Identify the blood parasite species.
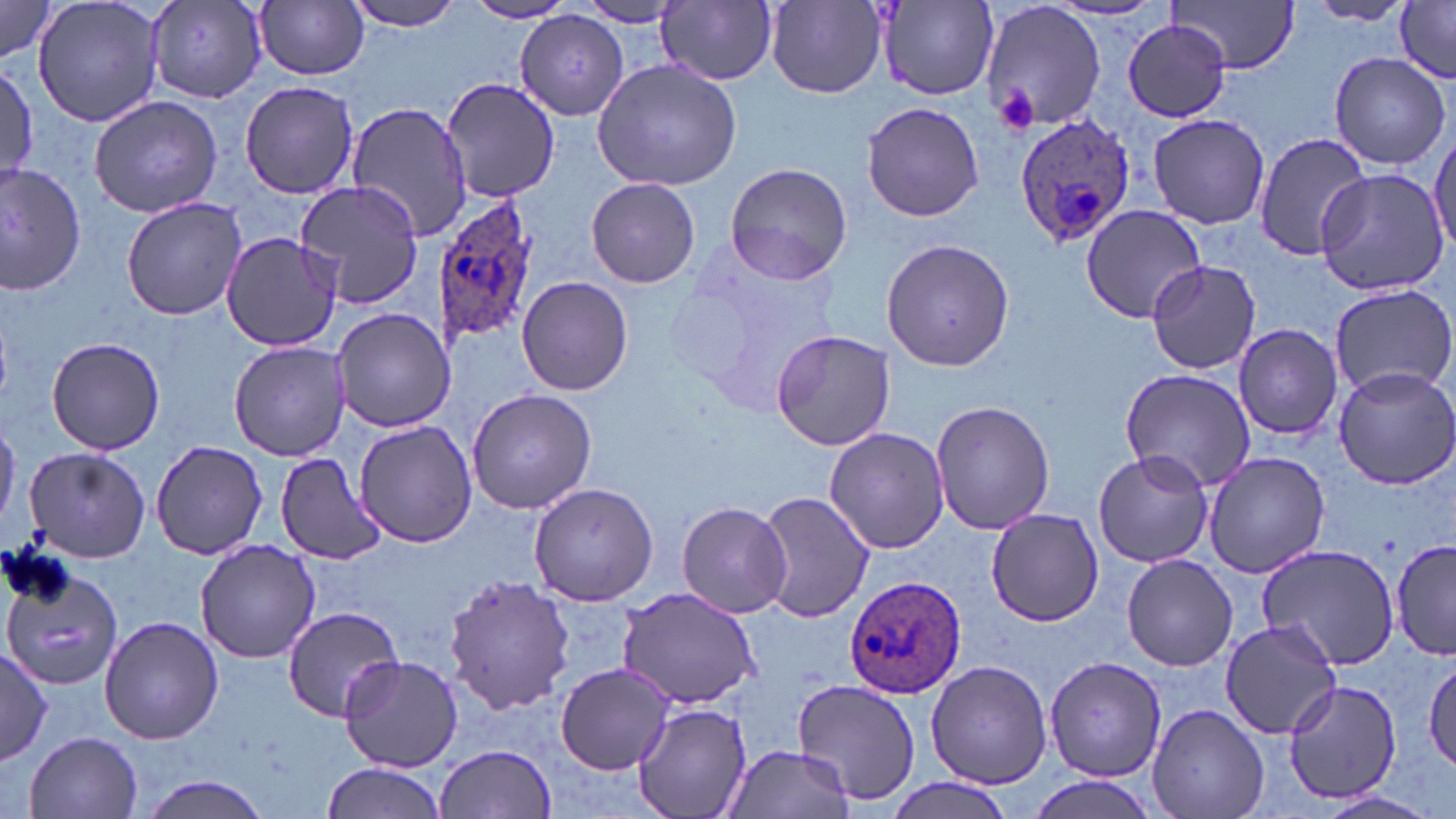
Plasmodium ovale.

image size = 1456×819 pixels
uninfected red blood cell locations = approximate bounding boxes as (x1, y1, x2, y2) in pixels: (31, 0, 165, 128), (345, 0, 471, 32), (876, 0, 997, 102), (145, 1, 270, 103), (767, 1, 888, 96), (981, 1, 1106, 135), (1168, 1, 1300, 74), (1301, 1, 1415, 24), (256, 2, 369, 80), (463, 2, 577, 24), (658, 2, 778, 85), (0, 3, 58, 64), (571, 3, 688, 27), (1394, 3, 1455, 82), (515, 12, 629, 121), (1122, 18, 1234, 122), (1331, 51, 1453, 171), (592, 59, 742, 191), (0, 65, 37, 187), (441, 78, 560, 205), (239, 80, 362, 199), (89, 95, 224, 218), (861, 100, 987, 223), (346, 101, 476, 242), (1146, 113, 1271, 230), (1251, 132, 1371, 259), (1429, 133, 1455, 256), (724, 162, 853, 284), (0, 166, 86, 294), (1317, 169, 1449, 296), (586, 177, 700, 288), (295, 179, 425, 309), (121, 198, 248, 319), (1081, 205, 1207, 321), (219, 231, 342, 351), (881, 238, 1015, 372), (664, 242, 847, 413), (1146, 260, 1261, 375), (516, 276, 632, 396), (1327, 283, 1456, 398), (330, 307, 455, 433), (1232, 322, 1345, 440), (770, 328, 896, 452), (48, 336, 165, 455), (229, 341, 348, 460), (1331, 366, 1456, 492), (1120, 368, 1256, 492), (467, 388, 597, 515), (930, 400, 1057, 536), (0, 414, 21, 531), (354, 420, 477, 547), (823, 427, 949, 554), (151, 439, 267, 560), (24, 446, 151, 563), (1092, 449, 1214, 568), (1203, 451, 1329, 577), (275, 453, 385, 564), (528, 482, 660, 606), (757, 491, 875, 622), (675, 499, 793, 618), (985, 508, 1101, 625), (1393, 538, 1456, 659), (195, 539, 323, 663), (1252, 542, 1401, 667), (1122, 555, 1238, 670), (0, 563, 128, 694), (445, 575, 574, 714), (617, 588, 765, 711), (281, 608, 407, 721), (99, 615, 223, 744), (1220, 618, 1345, 739), (0, 645, 51, 766), (339, 655, 463, 772), (1425, 656, 1456, 772), (1044, 657, 1168, 780), (925, 661, 1053, 789), (555, 662, 676, 773), (1282, 678, 1403, 805), (795, 679, 921, 806), (631, 701, 752, 819), (1147, 704, 1269, 819), (24, 731, 143, 818), (435, 744, 557, 819), (723, 744, 856, 819), (318, 762, 446, 819), (133, 774, 277, 818), (1025, 775, 1163, 819), (884, 779, 1017, 819), (1309, 790, 1443, 819)
platelet locations = approximate bounding boxes as (x1, y1, x2, y2) in pixels: (995, 84, 1040, 130)
preparation = thin blood film
field of view = single
modality = light microscopy
magnification = 1000x
stain = May-Grünwald-Giemsa
Plasmodium ovale-infected red blood cell locations = approximate bounding boxes as (x1, y1, x2, y2) in pixels: (1013, 112, 1137, 248), (433, 192, 543, 348), (844, 576, 969, 698)